State which parasite is depicted.
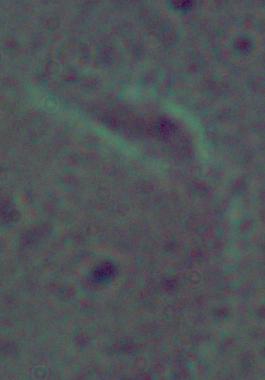
This is Leishmania.

modality = photomicrograph
magnification = 1000x